Point out each malaria parasite.
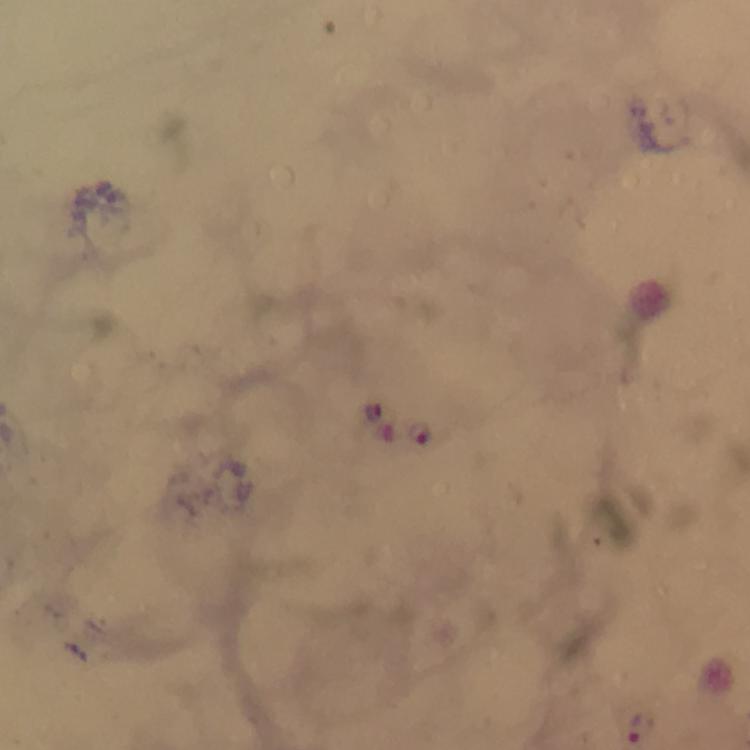
Approximate centers as {x, y} in pixels.
Malaria parasites: {108, 192}, {421, 431}, {643, 728}.

Immersion oil applied. From a malaria diagnostic workup. At 100x magnification. Cropped region of a single field of view. Smartphone photograph taken through a microscope. Image is 750×750 pixels. Thick smear. Giemsa-stained preparation.